Give the position of every Plasmodium parasite visible.
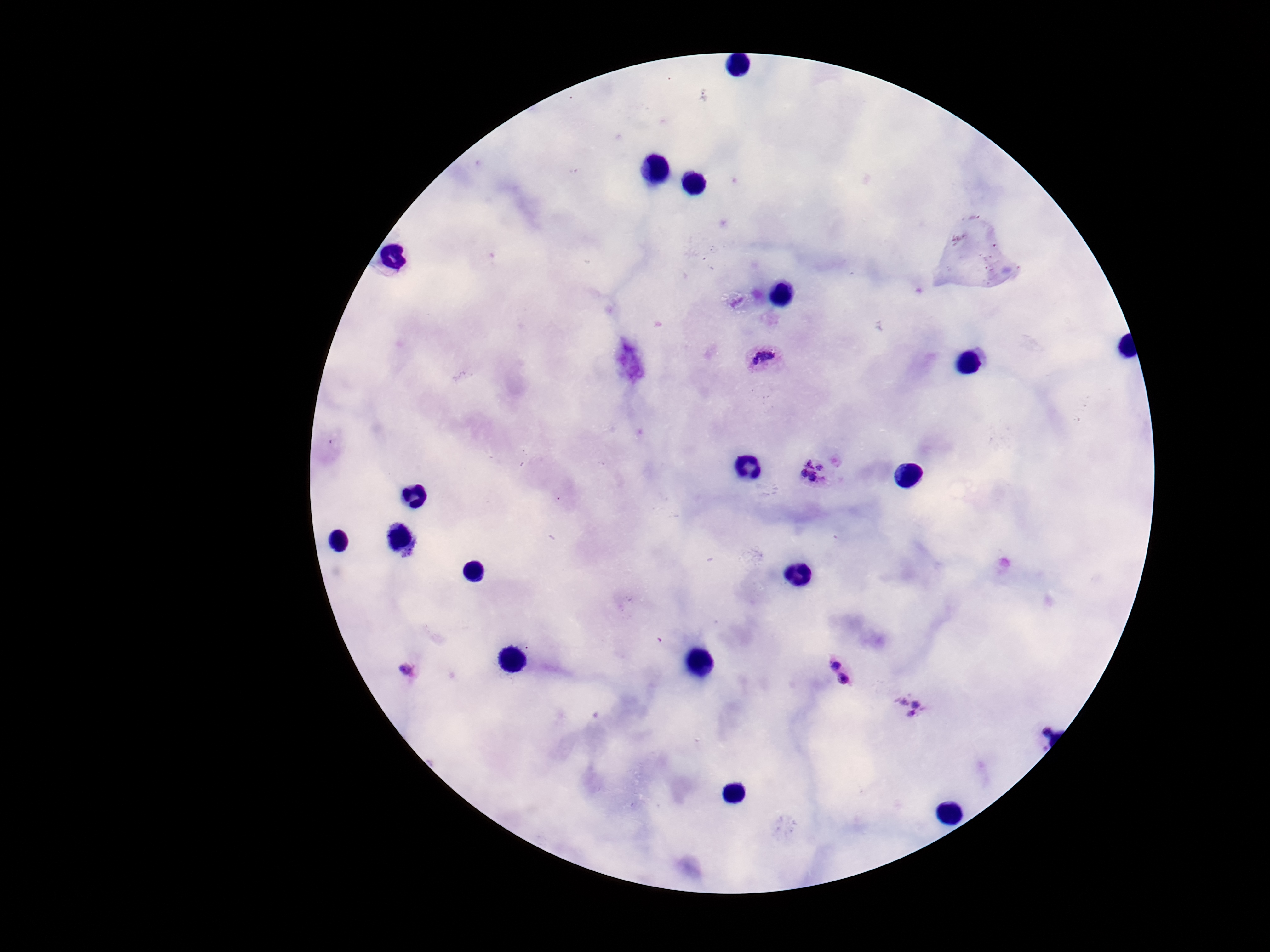
Approximate centers as {x, y} in pixels.
Plasmodium parasites: {764, 357}, {815, 471}, {834, 657}, {409, 673}, {844, 682}, {912, 703}, {1044, 725}.

Summary:
  - Capture: smartphone camera through the microscope eyepiece
  - Field of view: single
  - Patient malaria status: infected
  - Stain: Giemsa
  - Magnification: 100x
  - Preparation: thick peripheral-blood smear
  - Image size: 1270×952 pixels